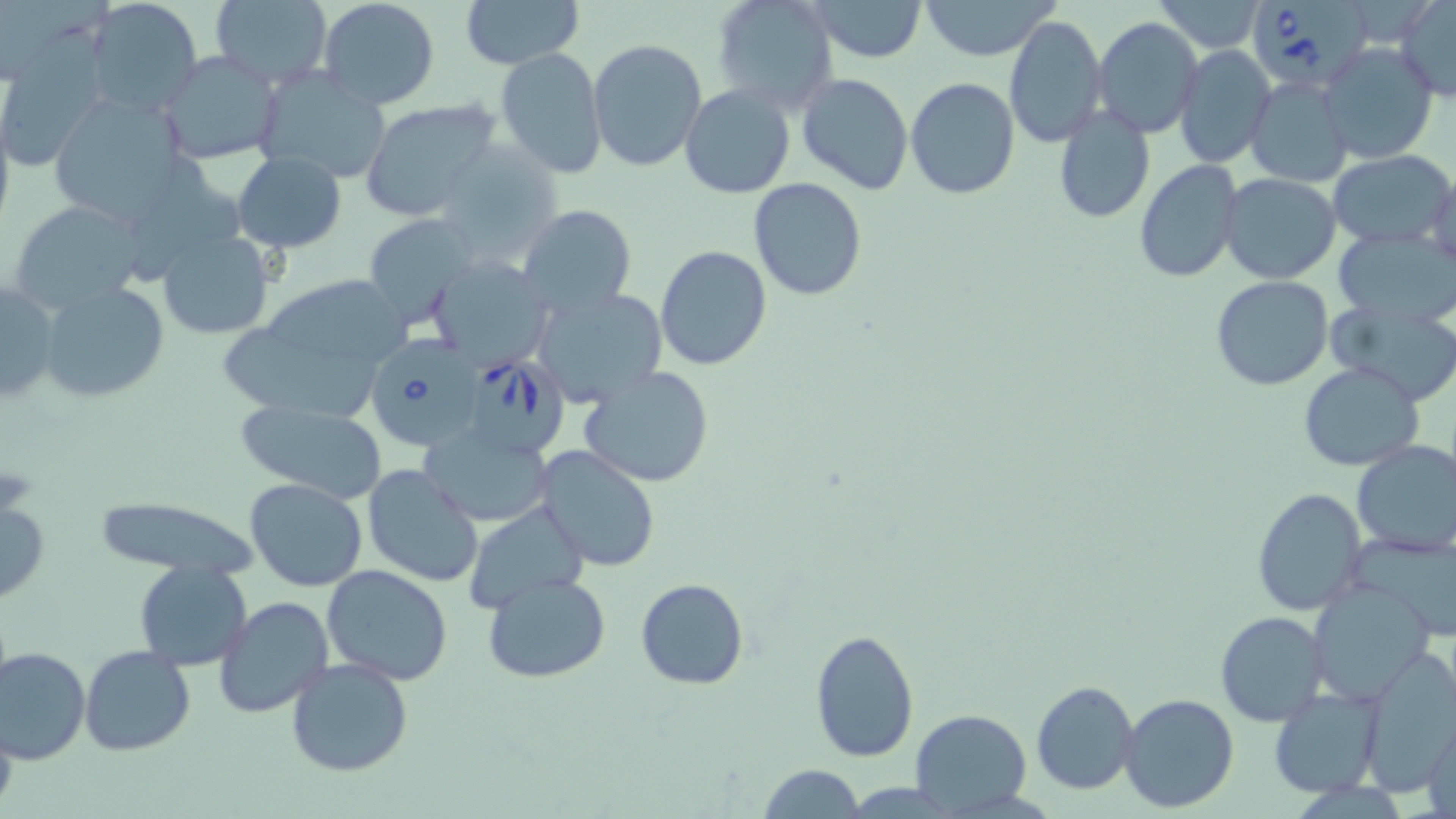
Approximate bounding boxes as (x1,y1)-(x2,y2) corner pairs in pixels. Babesia divergens-infected red blood cell locations: (1254,0)-(1377,97), (360,336)-(481,453), (467,354)-(575,459). Uninfected red blood cell locations: (317,0)-(441,110), (461,0)-(582,70), (711,0)-(839,115), (807,0)-(928,62), (918,0)-(1062,61), (1151,0)-(1268,53), (1395,0)-(1456,101), (83,1)-(203,118), (208,1)-(333,86), (1003,16)-(1107,149), (1094,16)-(1204,139), (276,24)-(417,161), (587,39)-(708,172), (1319,42)-(1438,164), (1174,44)-(1276,168), (496,47)-(607,178), (1,48)-(108,169), (159,50)-(283,164), (249,66)-(393,186), (796,72)-(914,195), (1246,75)-(1354,188), (905,76)-(1021,200), (680,85)-(796,199), (46,93)-(193,225), (359,101)-(498,222), (1052,106)-(1153,223), (433,142)-(562,266), (1326,150)-(1455,250), (231,151)-(346,253), (137,157)-(248,280), (1134,160)-(1242,282), (1424,172)-(1456,275), (1219,174)-(1342,285), (749,179)-(867,301), (10,199)-(149,313), (517,205)-(637,315), (365,216)-(480,328), (1334,228)-(1456,325), (157,231)-(275,340), (655,245)-(774,370), (428,256)-(553,373), (1209,276)-(1333,391), (1,281)-(61,410), (39,282)-(168,402), (269,284)-(413,362), (534,287)-(669,409), (1328,300)-(1456,404), (224,328)-(382,421), (1299,363)-(1424,472), (577,366)-(716,487), (235,396)-(387,502), (420,425)-(555,526), (1350,440)-(1456,558), (534,445)-(661,571), (362,464)-(484,587), (244,477)-(369,592), (1250,485)-(1367,617), (90,495)-(262,579), (461,499)-(592,612), (0,502)-(49,602), (134,561)-(251,669), (321,564)-(453,685), (483,573)-(612,682), (635,577)-(749,690), (1308,582)-(1436,705), (213,594)-(335,718), (1214,611)-(1328,727), (808,628)-(919,763), (80,645)-(196,756), (1,646)-(89,765), (1357,650)-(1456,792), (285,657)-(414,778), (1030,681)-(1139,796), (1268,687)-(1382,798), (1118,692)-(1240,813), (910,709)-(1031,814), (1422,714)-(1456,819), (0,715)-(17,814), (755,763)-(866,819). Slide-level diagnosis: Babesia divergens. Thin blood film. Light microscopy. May-Grünwald-Giemsa-stained preparation. One field of a larger specimen. Image is 1456×819 pixels. Captured at 1000x magnification.